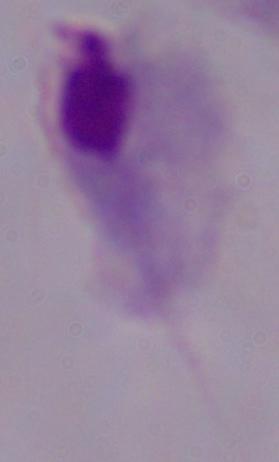
1000x magnification. A trichomonad is seen. Photomicrograph.